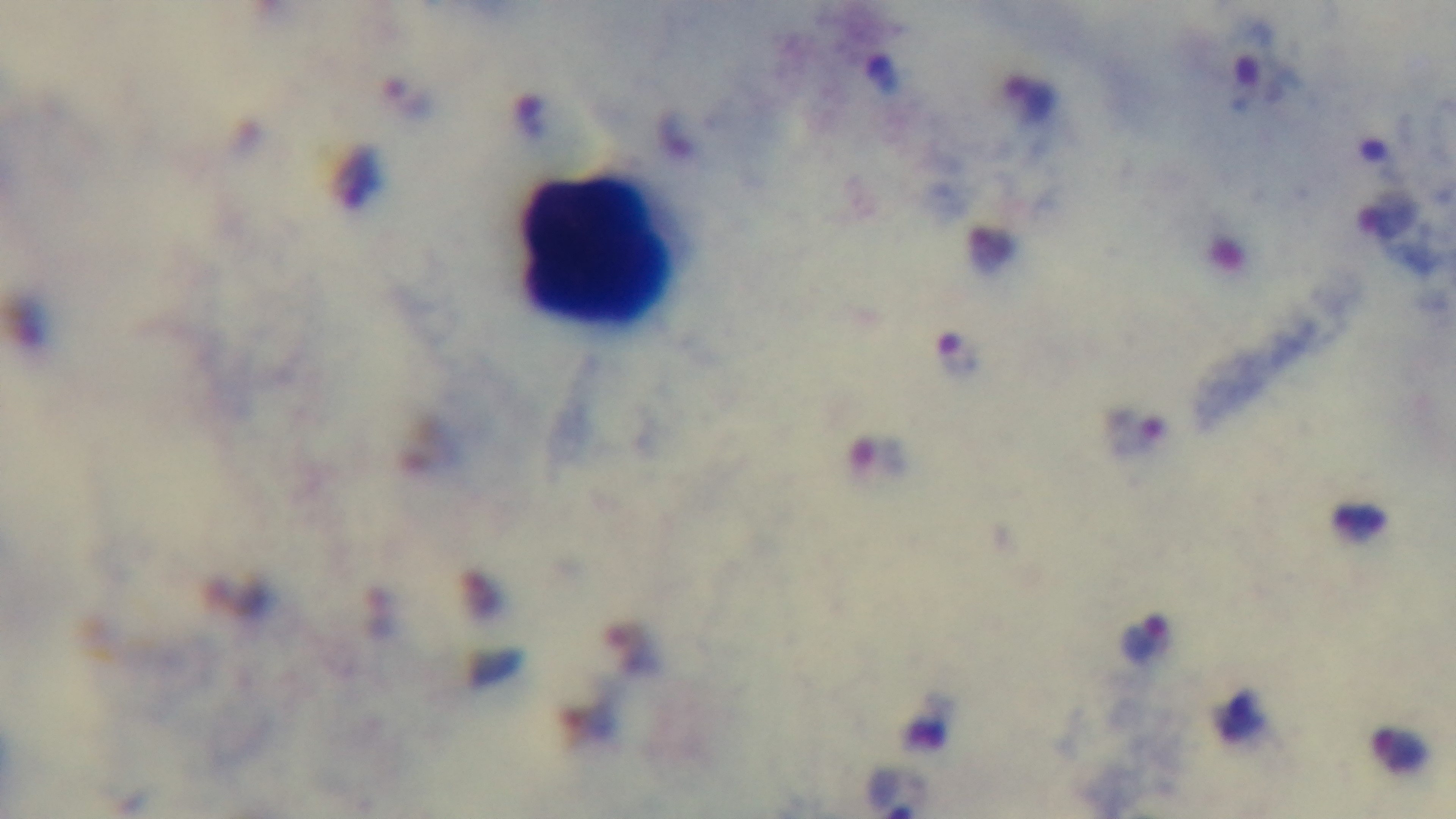 Giemsa-stained. Preparation: thick. Mounted 4K digital camera. Malaria status: infected. Light microscopy. Single field of view. 100x oil-immersion objective.